Describe the morphology of the red blood cells.
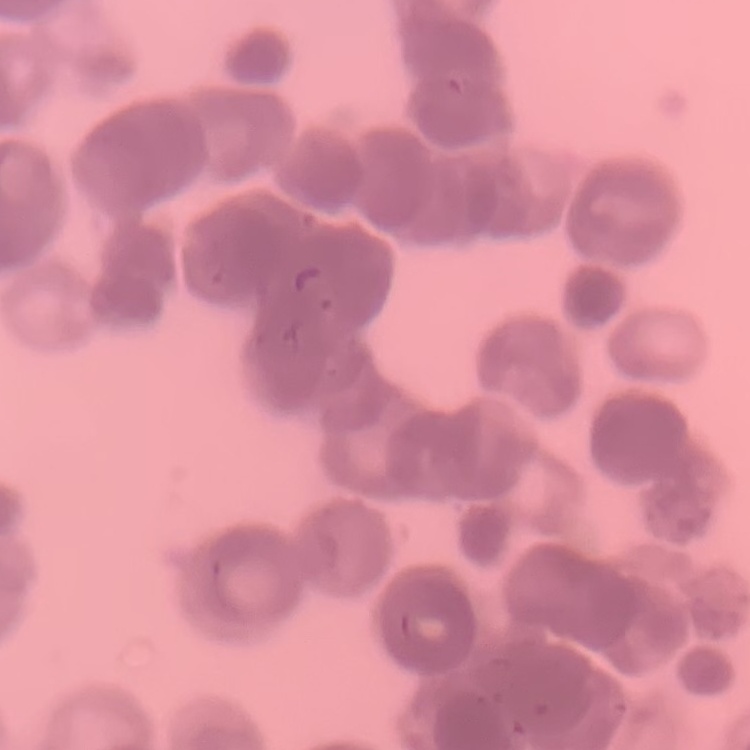
Rouleaux formation.

Summary:
  - Preparation: thin blood smear
  - Image type: square crop of a larger photomicrograph
  - Stain: Field's or Giemsa